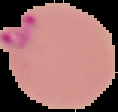

result = Plasmodium parasites detected
image type = cell region segmented out of the field of view; surrounding area masked to black
preparation = thin blood film
image size = 118×112 pixels